State the blood parasite species.
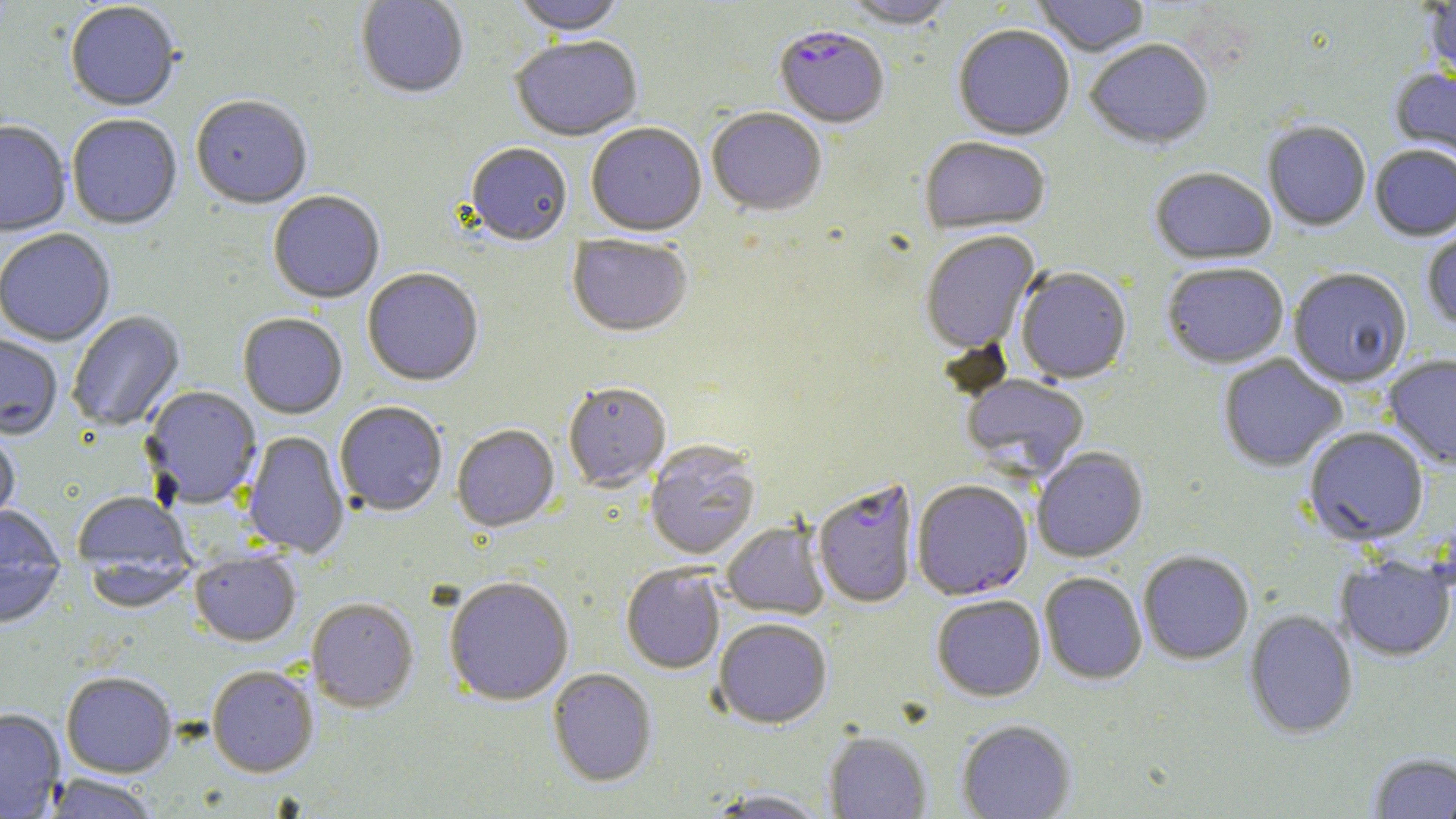

Plasmodium falciparum.

Summary:
  - Coordinate format: approximate bounding boxes as (x1,y1)-(x2,y2) corner pairs in pixels
  - Plasmodium falciparum-infected red blood cell locations: (774,29)-(889,130), (813,479)-(919,609), (911,480)-(1033,601)
  - Uninfected red blood cell locations: (356,0)-(469,100), (511,0)-(628,38), (1032,0)-(1150,58), (1422,0)-(1456,83), (841,1)-(958,31), (65,3)-(181,114), (953,26)-(1075,142), (510,38)-(644,143), (1085,41)-(1214,151), (1389,67)-(1456,169), (190,98)-(312,211), (707,109)-(826,217), (66,115)-(182,231), (0,122)-(71,237), (1263,123)-(1371,233), (586,125)-(706,237), (919,139)-(1050,237), (465,144)-(573,248), (1370,145)-(1456,242), (1150,169)-(1277,267), (268,193)-(385,305), (1422,219)-(1456,333), (0,230)-(116,346), (920,232)-(1040,355), (568,235)-(692,339), (1162,264)-(1289,370), (1015,268)-(1132,384), (1288,269)-(1412,389), (363,270)-(484,387), (67,311)-(185,432), (238,314)-(347,419), (0,333)-(63,440), (1218,354)-(1347,472), (1382,356)-(1456,471), (961,375)-(1090,479), (563,383)-(671,493), (141,386)-(262,509), (334,402)-(447,517), (452,425)-(560,533), (0,426)-(20,530), (1304,427)-(1430,546), (242,431)-(350,559), (644,442)-(761,560), (1032,448)-(1148,562), (72,492)-(194,577), (0,505)-(65,566), (722,522)-(830,620), (190,551)-(301,648), (1138,551)-(1254,665), (1336,556)-(1455,662), (83,561)-(197,613), (621,565)-(725,674), (0,566)-(64,630), (1039,572)-(1147,685), (443,577)-(574,707), (932,595)-(1046,702), (306,599)-(419,712), (1244,610)-(1358,740), (714,619)-(832,729), (207,666)-(318,778), (548,669)-(658,786), (61,671)-(177,778), (0,709)-(65,817), (956,720)-(1076,819), (824,732)-(931,818), (1368,752)-(1456,818), (43,774)-(161,819), (705,788)-(831,818)
  - Magnification: 1000x
  - Stain: May-Grünwald-Giemsa
  - Field of view: single
  - Preparation: thin blood film
  - Modality: optical microscopy
  - Image size: 1456×819 pixels